Assess the morphology of the red blood cells.
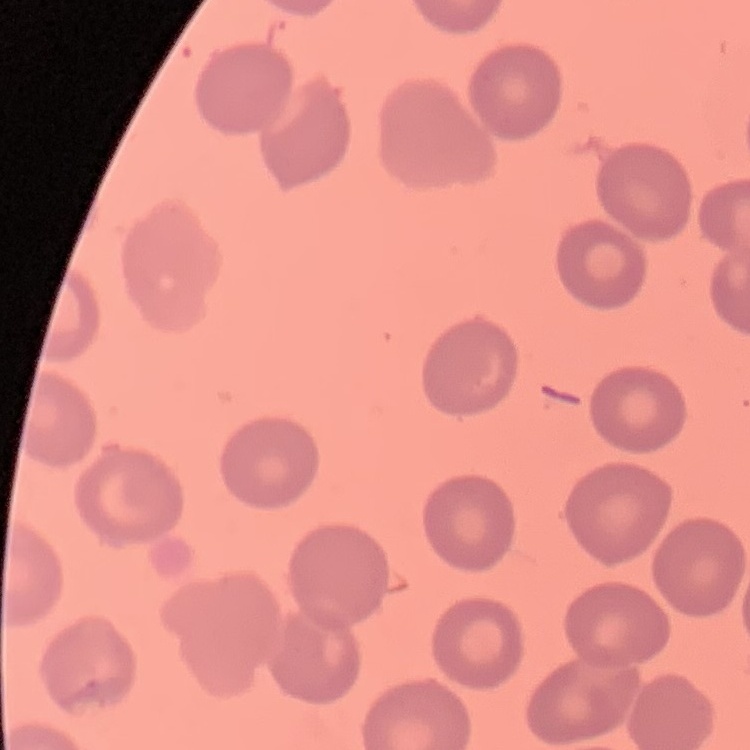

They show no rouleaux formation.

{
  "stain": "Field's or Giemsa",
  "preparation": "thin peripheral smear",
  "image_type": "square crop of a larger photomicrograph"
}